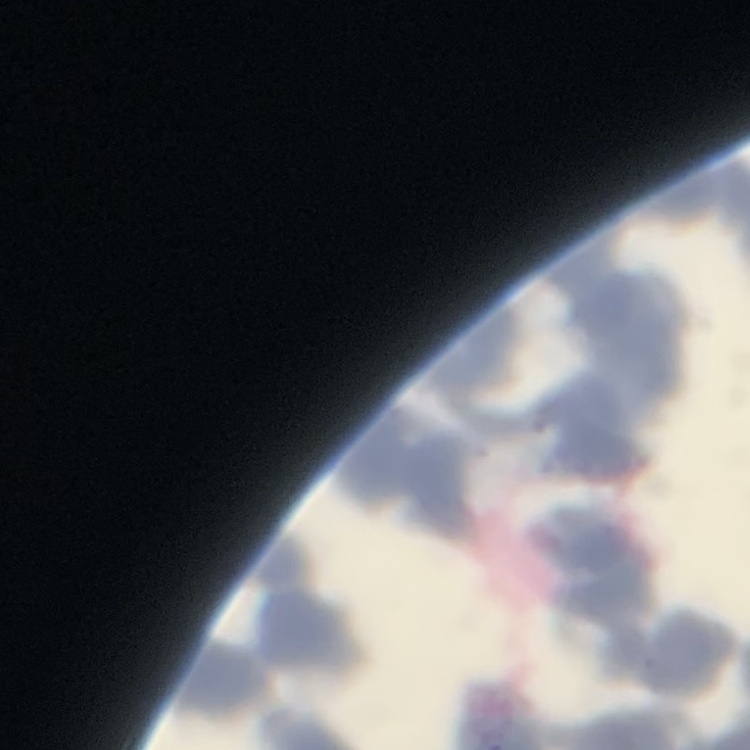

{
  "erythrocyte_morphology": "rouleaux formation",
  "stain": "Field's or Giemsa",
  "image_type": "square crop of a larger photomicrograph",
  "preparation": "thin peripheral smear"
}